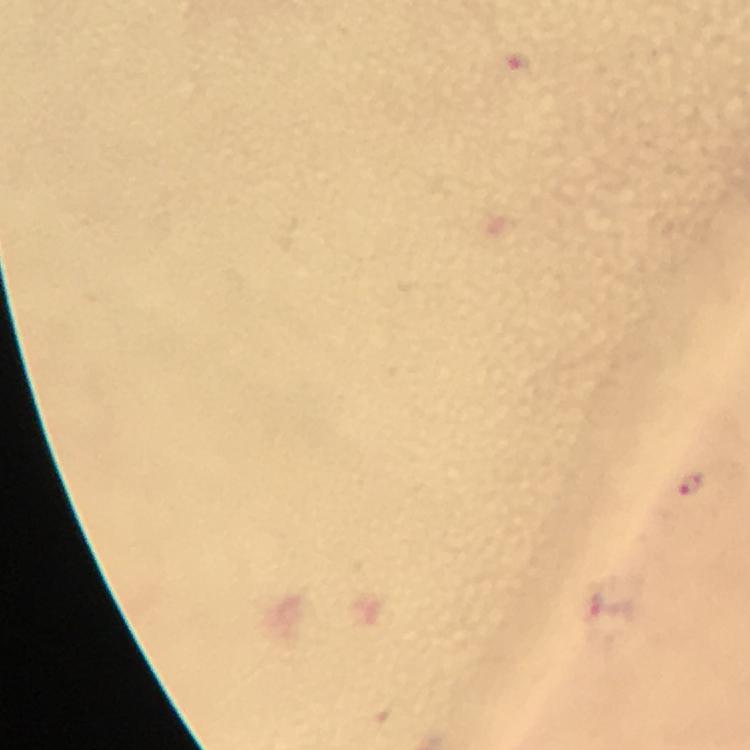 Approximate object centers, in pixels from the top-left corner. Plasmodium parasite locations: (x=518, y=61), (x=693, y=485). Giemsa-stained preparation. Immersion oil was used. Image is 750×750 pixels. 100x magnification. Thick smear. From a malaria diagnostic workup. Photographed with a smartphone mounted on the microscope. A crop from one field of view.